Mark where platelets are.
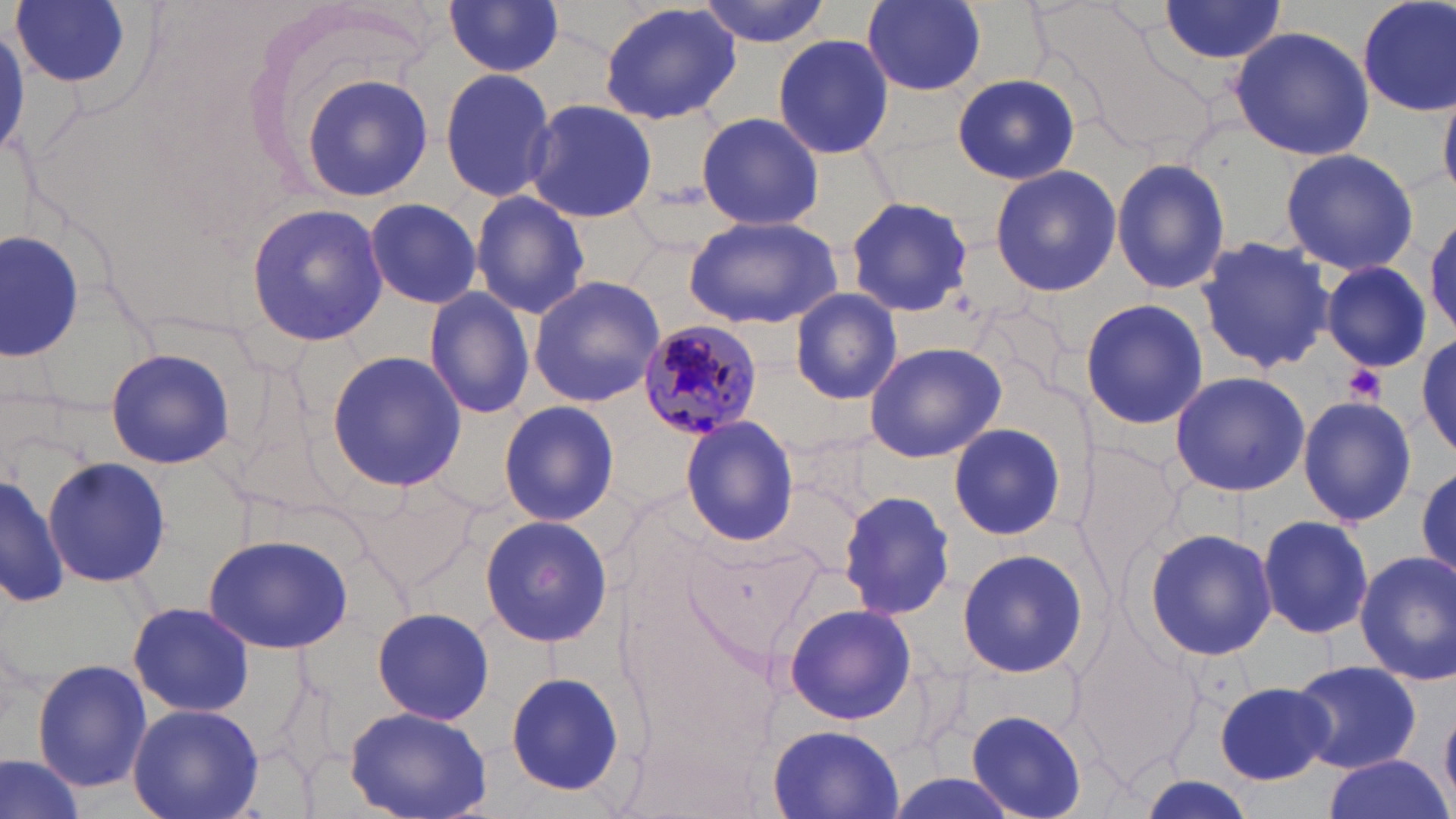
Approximate bounding boxes as (x1, y1, x2, y2) in pixels.
Platelets: (1344, 364, 1386, 404).

slide-level diagnosis = Plasmodium malariae
modality = light microscopy
uninfected red blood cell locations = approximate bounding boxes as (x1, y1, x2, y2) in pixels: (8, 0, 140, 97), (442, 0, 567, 81), (694, 0, 837, 46), (862, 0, 987, 94), (1357, 0, 1455, 117), (597, 1, 741, 127), (1153, 2, 1289, 65), (1228, 25, 1374, 161), (771, 32, 895, 160), (438, 67, 558, 205), (952, 72, 1080, 186), (300, 74, 433, 201), (1439, 80, 1456, 198), (523, 99, 659, 223), (695, 109, 823, 232), (1279, 147, 1421, 276), (1111, 157, 1231, 296), (987, 164, 1122, 297), (469, 190, 591, 320), (845, 196, 975, 318), (361, 199, 485, 311), (246, 200, 387, 346), (1427, 212, 1456, 336), (683, 214, 842, 330), (1, 231, 86, 362), (1195, 234, 1334, 374), (1322, 261, 1431, 373), (527, 275, 666, 408), (424, 287, 536, 419), (790, 289, 901, 402), (1079, 298, 1209, 431), (1417, 332, 1455, 455), (864, 340, 1007, 463), (104, 345, 238, 469), (326, 347, 466, 491), (1169, 371, 1311, 497), (1296, 394, 1418, 526), (495, 398, 621, 529), (679, 416, 801, 546), (948, 423, 1066, 541), (1073, 441, 1184, 593), (42, 457, 171, 588), (1413, 464, 1456, 586), (1, 469, 69, 609), (352, 480, 477, 591), (839, 491, 957, 620), (479, 514, 614, 648), (1256, 515, 1375, 640), (1141, 527, 1278, 662), (202, 533, 355, 654), (957, 548, 1089, 680), (1352, 552, 1456, 684), (126, 601, 255, 716), (783, 603, 916, 724), (369, 608, 498, 725), (31, 659, 151, 793), (1287, 659, 1424, 774), (504, 670, 625, 797), (1215, 682, 1334, 785), (127, 704, 263, 819), (344, 704, 494, 818), (965, 709, 1087, 817), (768, 725, 904, 817), (0, 750, 91, 819), (1319, 755, 1453, 819)
image size = 1456×819 pixels
magnification = 1000x
Plasmodium malariae-infected red blood cell locations = approximate bounding boxes as (x1, y1, x2, y2) in pixels: (637, 319, 765, 439)
preparation = thin blood film
stain = May-Grünwald-Giemsa
field of view = single